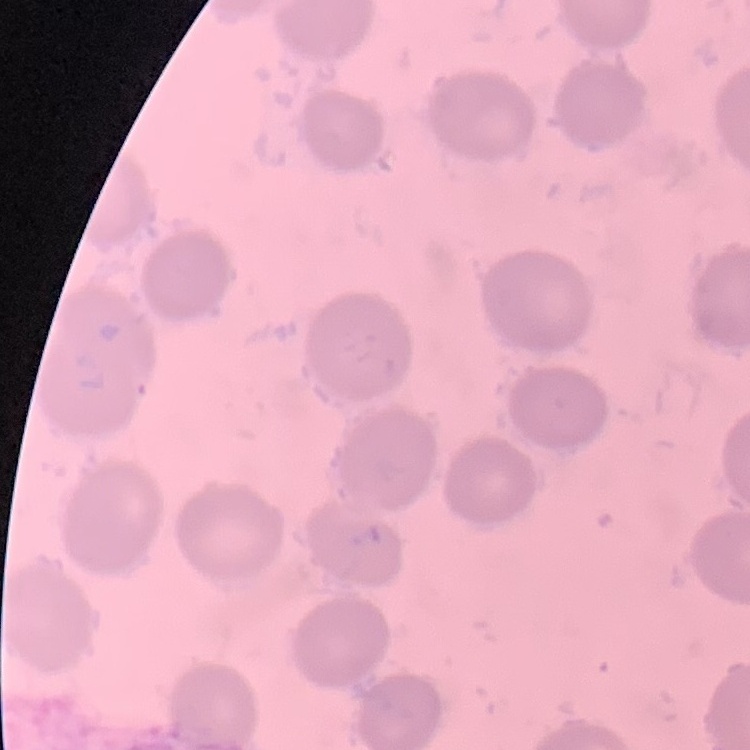

The red blood cells exhibit no rouleaux formation. One tile cut from a larger photomicrograph. Thin peripheral smear. Stained with either Field's or Giemsa.